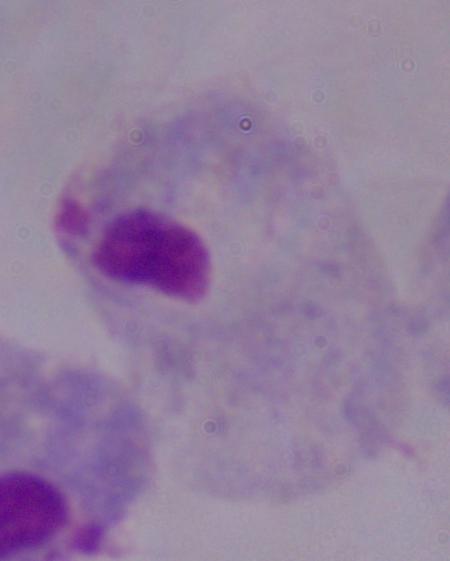

Photomicrograph. Captured at 1000x magnification. A trichomonad is seen.